Identify the cell.
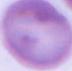

This is an erythrocyte.

magnification: 1000x
modality: photomicrograph